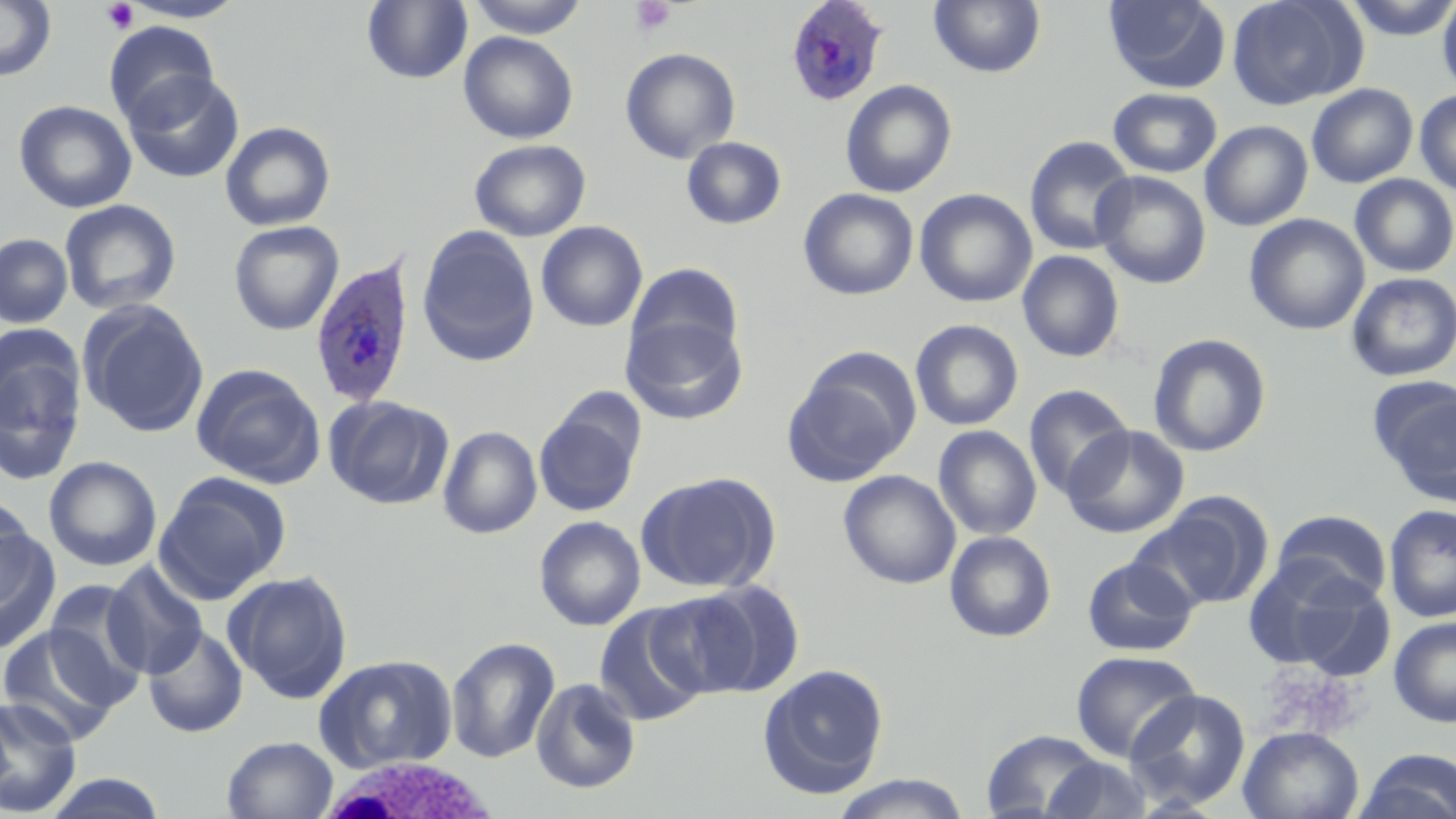

Approximate bounding boxes as (x1, y1, x2, y2) in pixels. White blood cell locations: (313, 756, 506, 819). Platelet locations: (630, 0, 676, 37), (101, 1, 139, 34), (1261, 665, 1363, 739). Plasmodium ovale-infected red blood cell locations: (785, 1, 889, 107), (308, 253, 416, 410). Uninfected red blood cell locations: (0, 0, 57, 83), (117, 0, 250, 23), (465, 0, 590, 38), (1103, 0, 1231, 93), (1226, 0, 1363, 109), (1341, 0, 1456, 41), (1437, 0, 1456, 97), (362, 1, 472, 84), (929, 1, 1046, 78), (103, 21, 220, 129), (459, 32, 578, 144), (620, 47, 740, 164), (122, 71, 244, 184), (840, 80, 957, 198), (1306, 83, 1419, 188), (1108, 87, 1223, 178), (1414, 89, 1456, 195), (14, 100, 137, 213), (1200, 120, 1313, 231), (220, 122, 336, 232), (681, 136, 787, 230), (1024, 136, 1137, 256), (469, 139, 591, 241), (1092, 171, 1211, 288), (1350, 174, 1456, 277), (798, 188, 919, 300), (915, 188, 1037, 307), (59, 199, 182, 315), (1245, 213, 1370, 335), (228, 220, 344, 336), (536, 221, 648, 332), (416, 225, 540, 366), (0, 233, 73, 328), (1017, 250, 1125, 362), (626, 262, 744, 365), (1346, 272, 1456, 381), (78, 300, 210, 438), (621, 314, 748, 425), (910, 319, 1024, 431), (1148, 333, 1272, 458), (0, 335, 88, 487), (784, 350, 920, 486), (190, 363, 326, 489), (1372, 379, 1456, 502), (1023, 384, 1133, 499), (324, 394, 453, 510), (534, 399, 645, 517), (1063, 424, 1189, 539), (933, 425, 1042, 540), (437, 426, 542, 539), (43, 456, 163, 571), (838, 469, 961, 589), (636, 471, 778, 593), (154, 472, 291, 604), (1146, 491, 1273, 611), (0, 493, 35, 604), (1383, 504, 1456, 623), (1272, 510, 1392, 605), (534, 515, 646, 631), (0, 517, 61, 654), (944, 531, 1056, 642), (1242, 555, 1374, 671), (1082, 556, 1198, 656), (103, 561, 210, 679), (223, 570, 354, 703), (42, 578, 150, 706), (673, 579, 806, 699), (594, 605, 709, 727), (1389, 617, 1456, 727), (0, 625, 124, 744), (142, 625, 248, 738), (446, 636, 560, 763), (1069, 650, 1201, 763), (314, 654, 458, 774), (757, 663, 890, 799), (530, 677, 642, 794), (1124, 689, 1251, 809), (0, 696, 82, 817), (1238, 726, 1363, 819), (981, 730, 1107, 818), (222, 736, 338, 819), (1354, 748, 1456, 819), (1040, 756, 1154, 818), (39, 772, 169, 818), (830, 774, 972, 818). Slide-level diagnosis: Plasmodium ovale. Light microscopy. May-Grünwald-Giemsa stain. Thin blood film. Image is 1456×819 pixels. Captured at 1000x magnification. One field of a larger specimen.